State the blood parasite species.
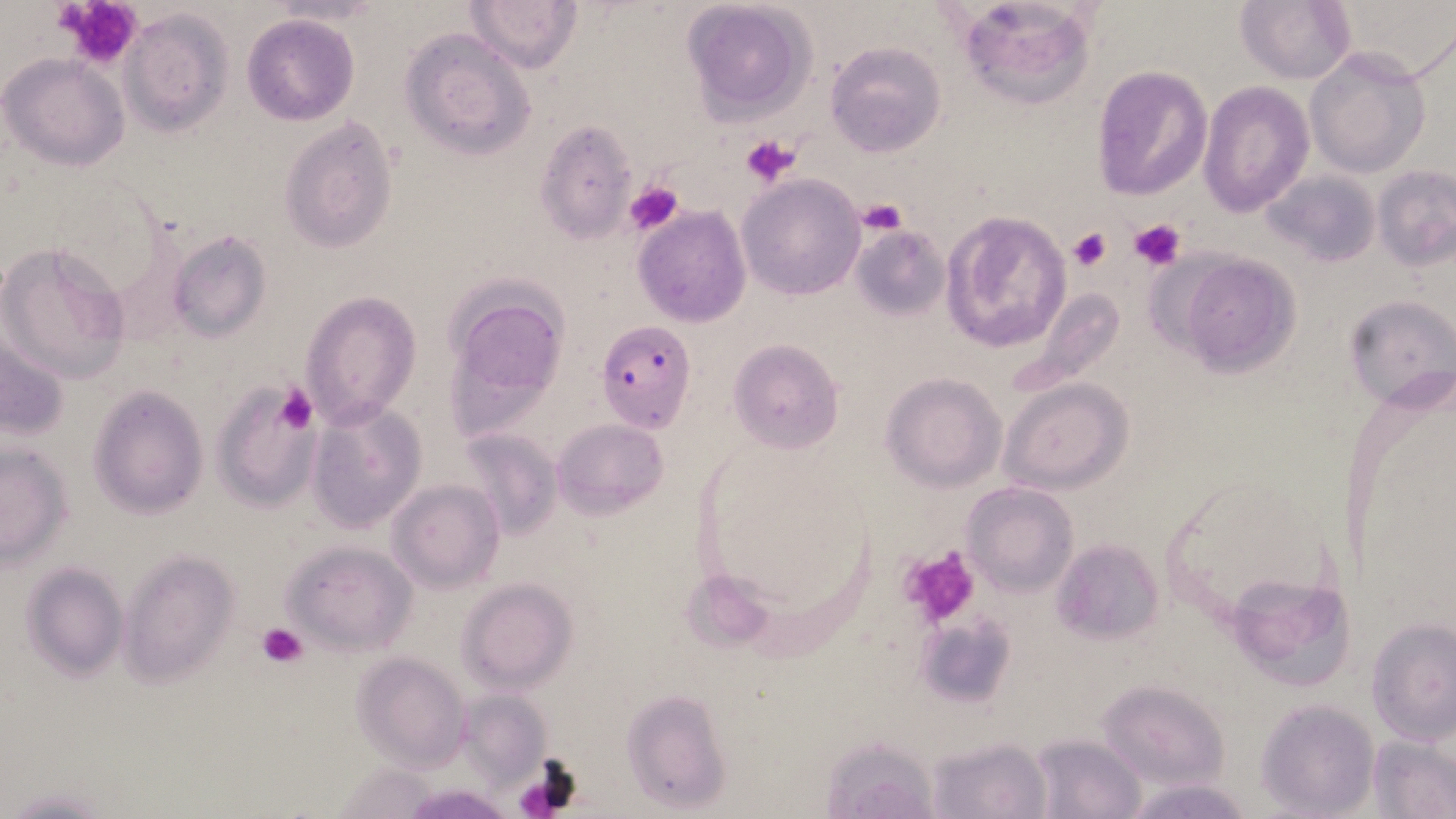
Plasmodium falciparum.

stain = May-Grünwald-Giemsa
Plasmodium falciparum-infected red blood cell locations = approximate bounding boxes as (x1,y1)-(x2,y2) corner pairs in pixels: (596,322)-(696,432)
uninfected red blood cell locations = approximate bounding boxes as (x1,y1)-(x2,y2) corner pairs in pixels: (956,0)-(1098,111), (464,1)-(581,73), (681,1)-(815,121), (1236,2)-(1354,83), (118,10)-(235,135), (242,15)-(359,125), (397,29)-(535,158), (825,41)-(946,156), (1303,46)-(1432,177), (2,56)-(128,170), (1091,66)-(1212,201), (1198,80)-(1315,217), (278,116)-(400,254), (534,120)-(638,243), (1374,165)-(1455,270), (1265,169)-(1380,268), (737,174)-(866,300), (633,206)-(751,327), (941,210)-(1070,354), (850,225)-(950,320), (167,231)-(272,342), (0,239)-(131,383), (1175,252)-(1303,377), (453,283)-(572,373), (1027,287)-(1125,391), (298,289)-(423,429), (1345,294)-(1455,413), (448,307)-(556,429), (0,330)-(69,448), (729,338)-(845,454), (880,373)-(1007,492), (999,378)-(1134,494), (212,379)-(318,514), (89,386)-(208,518), (307,401)-(427,533), (553,417)-(667,518), (457,429)-(561,537), (0,444)-(73,566), (388,478)-(505,591), (962,481)-(1079,596), (1052,539)-(1164,644), (284,541)-(418,657), (118,549)-(240,685), (22,563)-(128,680), (682,570)-(778,651), (1239,575)-(1358,685), (456,577)-(578,694), (1368,616)-(1455,745), (921,619)-(1014,702), (352,653)-(472,772), (1098,682)-(1232,790), (622,690)-(731,809), (1257,699)-(1380,818), (1029,733)-(1148,819), (1369,733)-(1455,819), (928,735)-(1051,818), (820,737)-(942,819), (1125,779)-(1254,817), (3,787)-(121,816)
modality = optical microscopy
field of view = single
magnification = 1000x
platelet locations = approximate bounding boxes as (x1,y1)-(x2,y2) corner pairs in pixels: (55,0)-(144,68), (740,133)-(801,187), (624,180)-(684,238), (856,198)-(908,237), (1128,218)-(1186,270), (1067,226)-(1113,271), (275,383)-(319,432), (898,545)-(982,626), (259,622)-(309,669), (514,761)-(580,815)
preparation = thin blood smear
image size = 1456×819 pixels